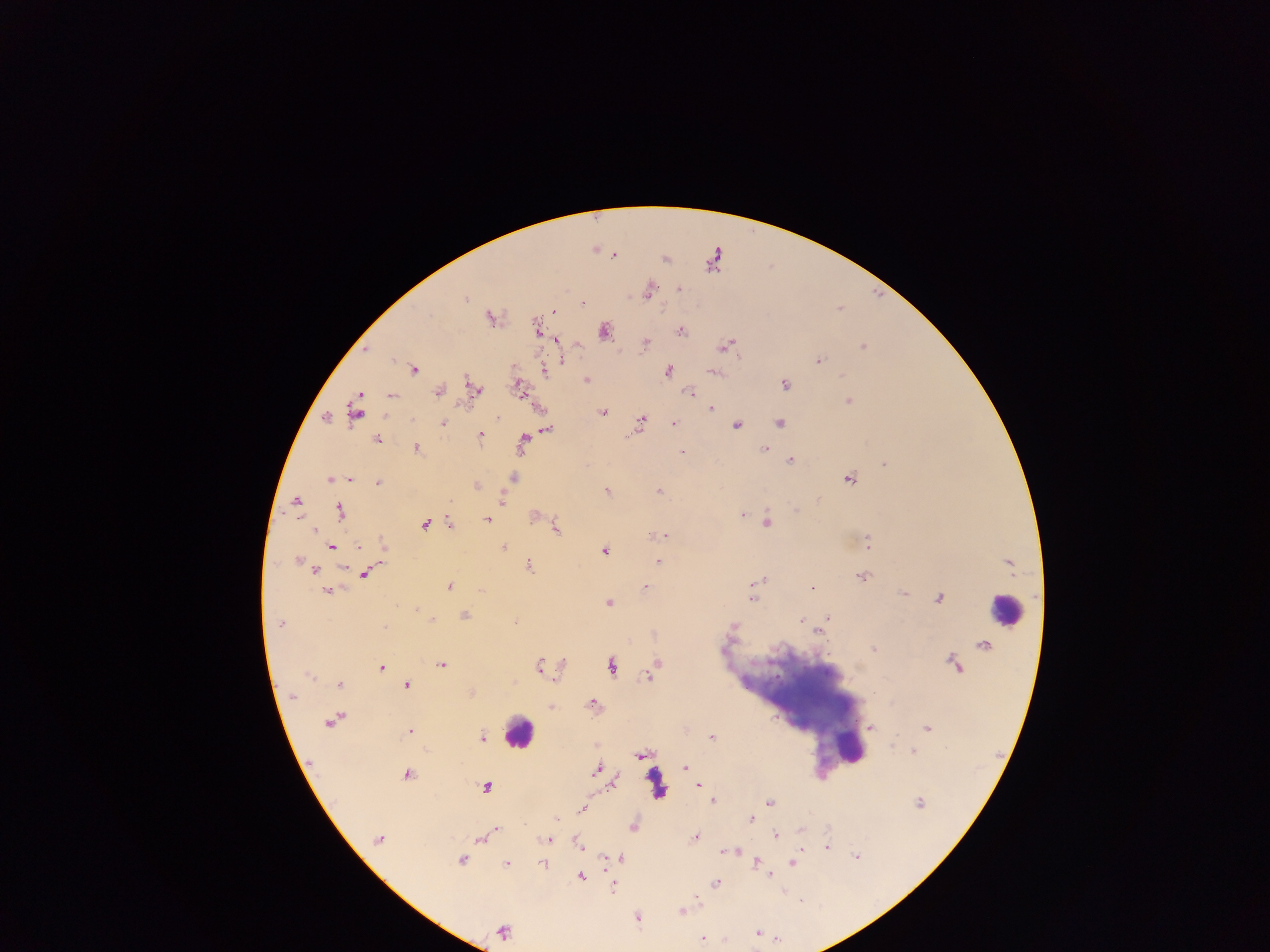

Approximate centers as [x, y] in pixels. Malaria parasite locations: [595, 249], [614, 255], [664, 258], [679, 289], [647, 290], [463, 297], [582, 304], [553, 311], [490, 316], [535, 328], [604, 330], [680, 331], [556, 341], [644, 342], [725, 345], [862, 346], [364, 350], [561, 354], [563, 360], [818, 360], [414, 369], [544, 370], [667, 371], [713, 372], [843, 375], [585, 379], [784, 384], [475, 388], [519, 388], [438, 392], [688, 392], [392, 396], [848, 401], [709, 408], [539, 409], [355, 410], [602, 411], [496, 416], [326, 417], [441, 423], [641, 423], [779, 423], [672, 424], [735, 425], [546, 428], [479, 435], [377, 440], [522, 443], [417, 448], [764, 450], [681, 452], [789, 461], [884, 464], [513, 478], [848, 478], [330, 479], [349, 480], [378, 482], [476, 485], [606, 491], [658, 491], [502, 501], [296, 502], [340, 511], [797, 511], [741, 514], [534, 515], [747, 516], [486, 519], [766, 522], [424, 524], [449, 524], [555, 527], [313, 529], [661, 535], [867, 544], [382, 545], [503, 546], [331, 547], [604, 550], [380, 558], [297, 560], [658, 561], [1008, 563], [528, 567], [313, 570], [363, 573], [861, 577], [757, 580], [448, 586], [645, 586], [754, 588], [812, 588], [481, 589], [327, 591], [903, 593], [939, 597], [751, 598], [608, 602], [463, 615], [828, 617], [432, 619], [799, 620], [280, 623], [822, 627], [818, 630], [982, 645], [874, 648], [954, 664], [440, 665], [538, 665], [561, 665], [610, 665], [655, 665], [382, 667], [649, 674], [309, 675], [339, 684], [406, 684], [470, 693], [291, 697], [592, 704], [551, 707], [333, 720], [869, 726], [926, 727], [409, 731], [711, 737], [481, 738], [913, 751], [642, 754], [684, 767], [597, 769], [406, 774], [613, 781], [697, 785], [485, 787], [712, 800], [769, 802], [918, 803], [581, 809], [557, 819], [749, 819], [632, 826], [799, 828], [495, 829], [775, 834], [479, 837], [694, 837], [548, 839], [379, 840], [577, 842], [826, 847], [732, 850], [725, 851], [855, 855], [621, 858], [463, 860], [608, 860], [757, 862], [792, 862], [543, 863], [507, 864], [770, 875], [580, 876], [715, 883], [612, 885], [681, 911], [636, 917], [503, 931], [755, 932], [702, 938]. Leukocyte locations: [1006, 611], [794, 698], [518, 732], [851, 748], [656, 784]. Thick blood smear. Photographed through a microscope with a mobile-phone camera. Sample from Ghana. One field of view. Image is 1270×952 pixels.